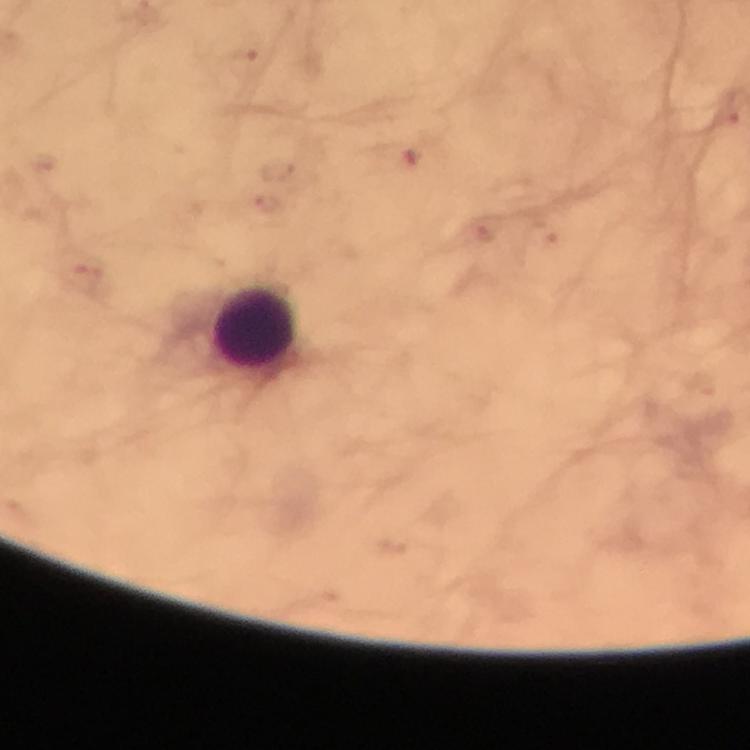

Approximate centers as {x, y} in pixels.
Summary:
  - Leukocyte locations: {256, 326}
  - Malaria parasite locations: {244, 60}, {411, 160}, {280, 169}, {268, 205}, {481, 233}, {539, 234}
  - Stain: Giemsa
  - Cropped from: one field of view
  - Capture: smartphone camera through the microscope
  - Magnification: 100x
  - Context: from a malaria diagnostic workup
  - Immersion oil: applied
  - Preparation: thick blood film
  - Image size: 750×750 pixels